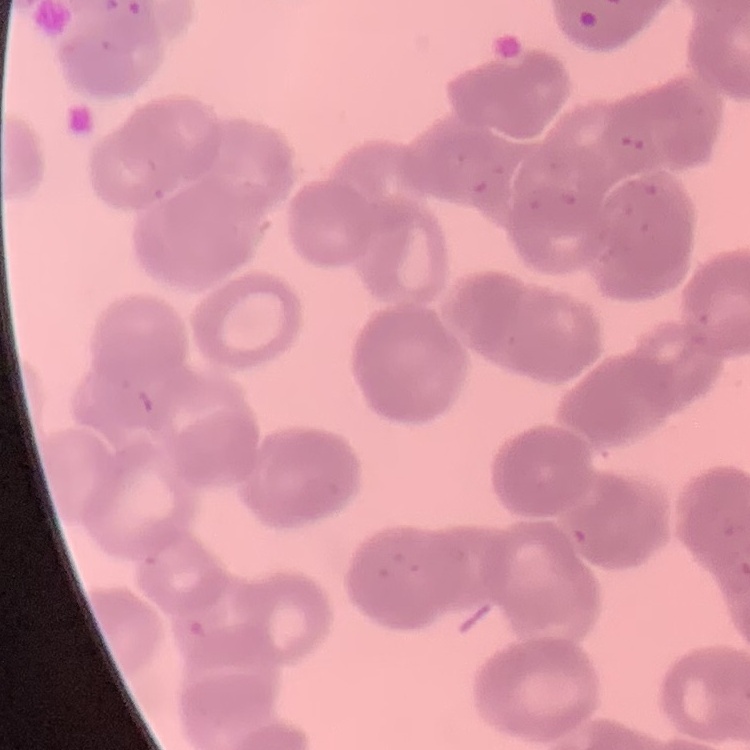
Summary:
  - Red blood cell morphology: rouleaux formation
  - Image type: square crop of a larger photomicrograph
  - Stain: Field's or Giemsa
  - Preparation: thin blood film